Classify this cell by malaria status.
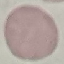
Uninfected.

Automatically extracted cell patch, resized to 64 × 64 pixels. Photographed with a smartphone camera at the microscope eyepiece. Giemsa-stained preparation. Thin blood film.